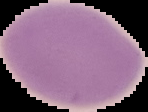
result = no Plasmodium parasites seen
image size = 148×112 pixels
preparation = thin blood smear
image type = cell region segmented out of the field of view; surrounding area masked to black